Comment on the morphology of the red blood cells.
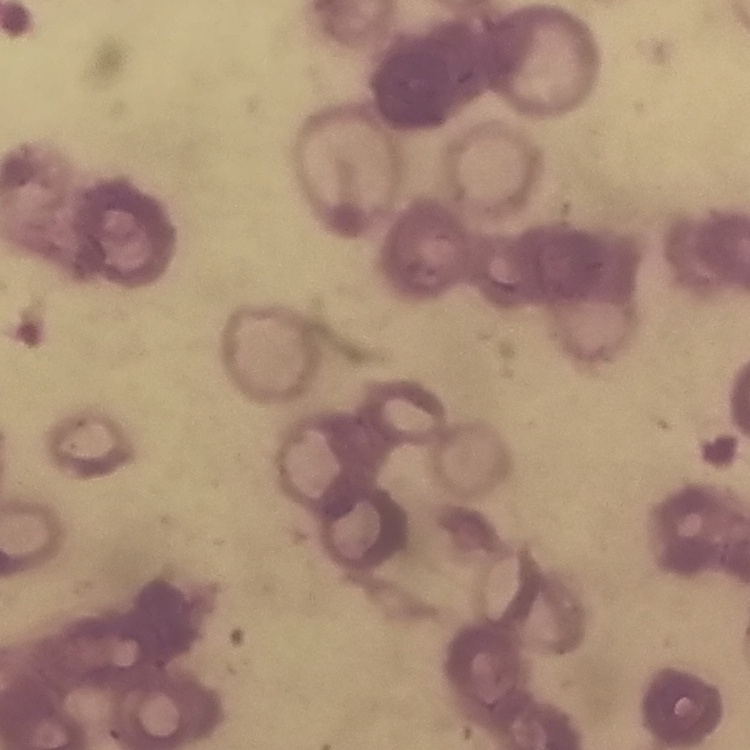
Rouleaux formation.

Thin peripheral smear. Field's or Giemsa stain. Square crop of a larger photomicrograph.